Look for Plasmodium parasites.
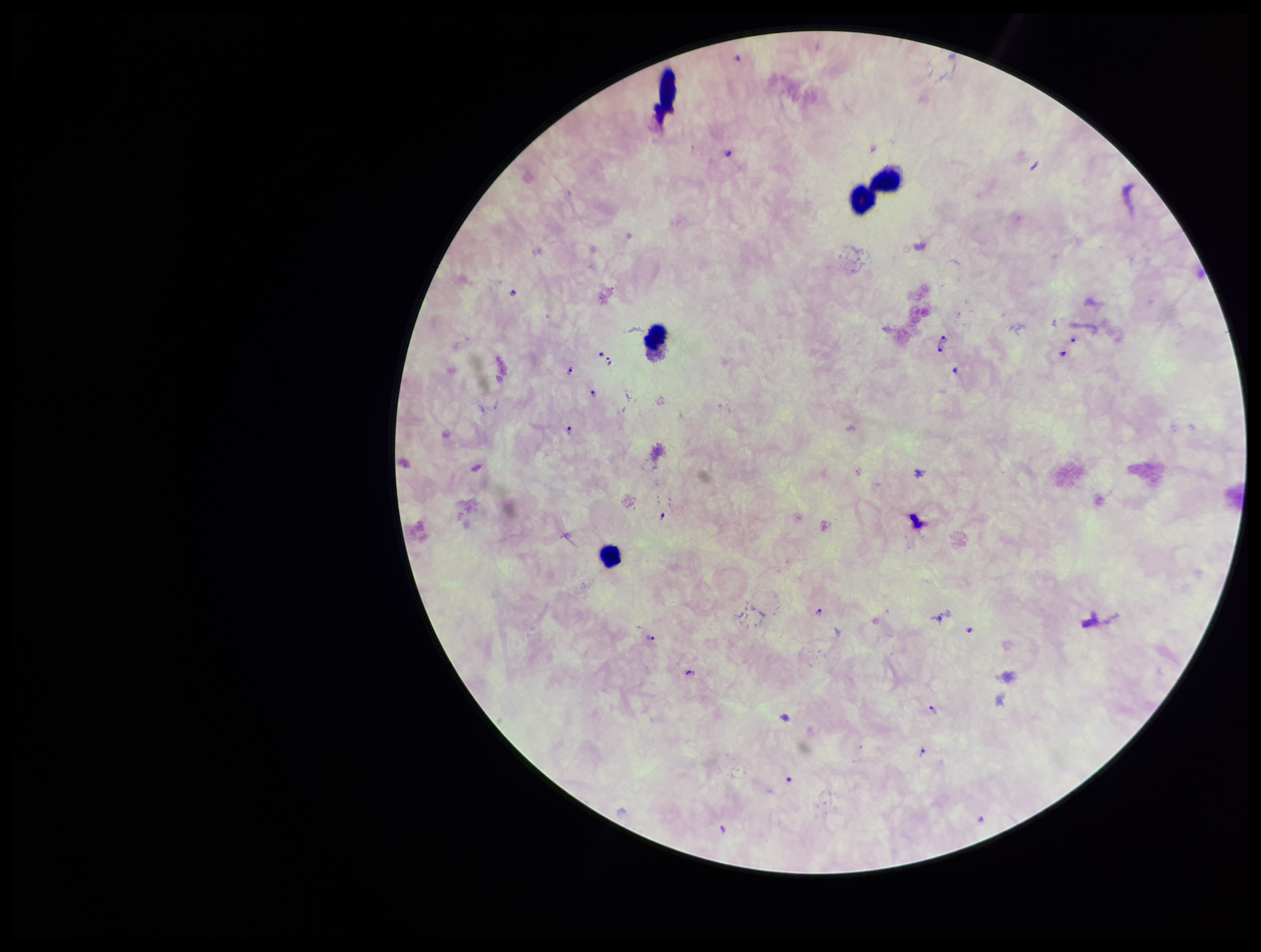

Detected.

field of view = one from this slide
leukocyte count = 4
patient malaria status = positive
capture = smartphone photograph through the microscope eyepiece
species reported for this patient = Plasmodium falciparum
preparation = thick smear
image size = 1261×952 pixels
parasite count = 17
stain = Giemsa